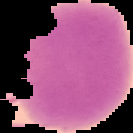
image_size: 133×133 pixels
result: no Plasmodium parasites seen
preparation: thin blood film
image_type: cell region segmented out of the field of view; surrounding area masked to black